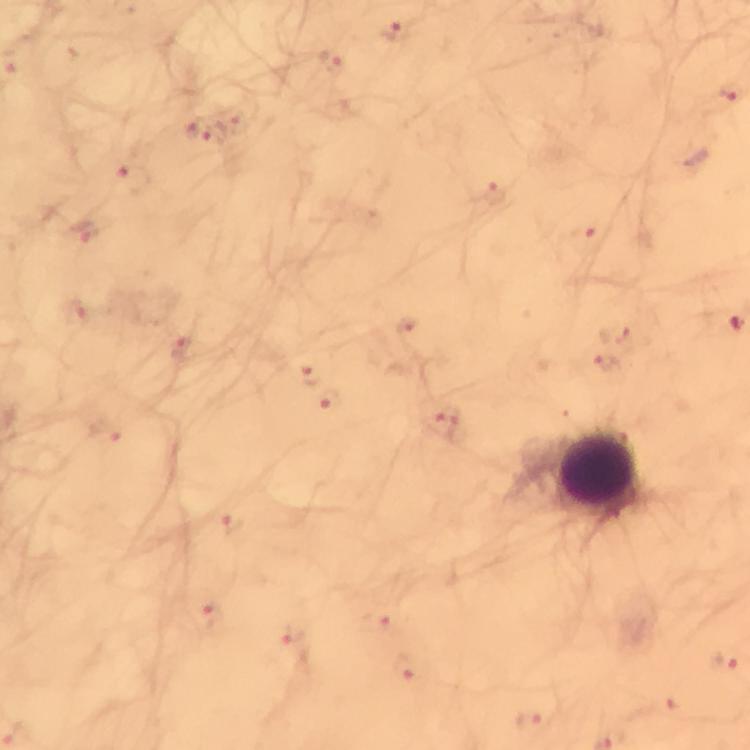

stain = Giemsa
cropped from = a single field of view
magnification = 100x
Plasmodium parasite locations = approximate centers as {x, y} in pixels: {391, 32}, {330, 62}, {730, 93}, {234, 125}, {199, 131}, {133, 179}, {494, 193}, {85, 228}, {590, 237}, {77, 316}, {406, 327}, {179, 349}, {611, 367}, {309, 376}, {328, 399}, {444, 421}, {103, 431}, {232, 524}, {208, 616}, {379, 619}, {294, 634}, {725, 660}, {404, 667}, {531, 722}
leukocyte locations = approximate centers as {x, y} in pixels: {599, 474}
capture = smartphone mounted on the microscope
preparation = thick blood film
context = from a malaria diagnostic workup
immersion oil = used
image size = 750×750 pixels